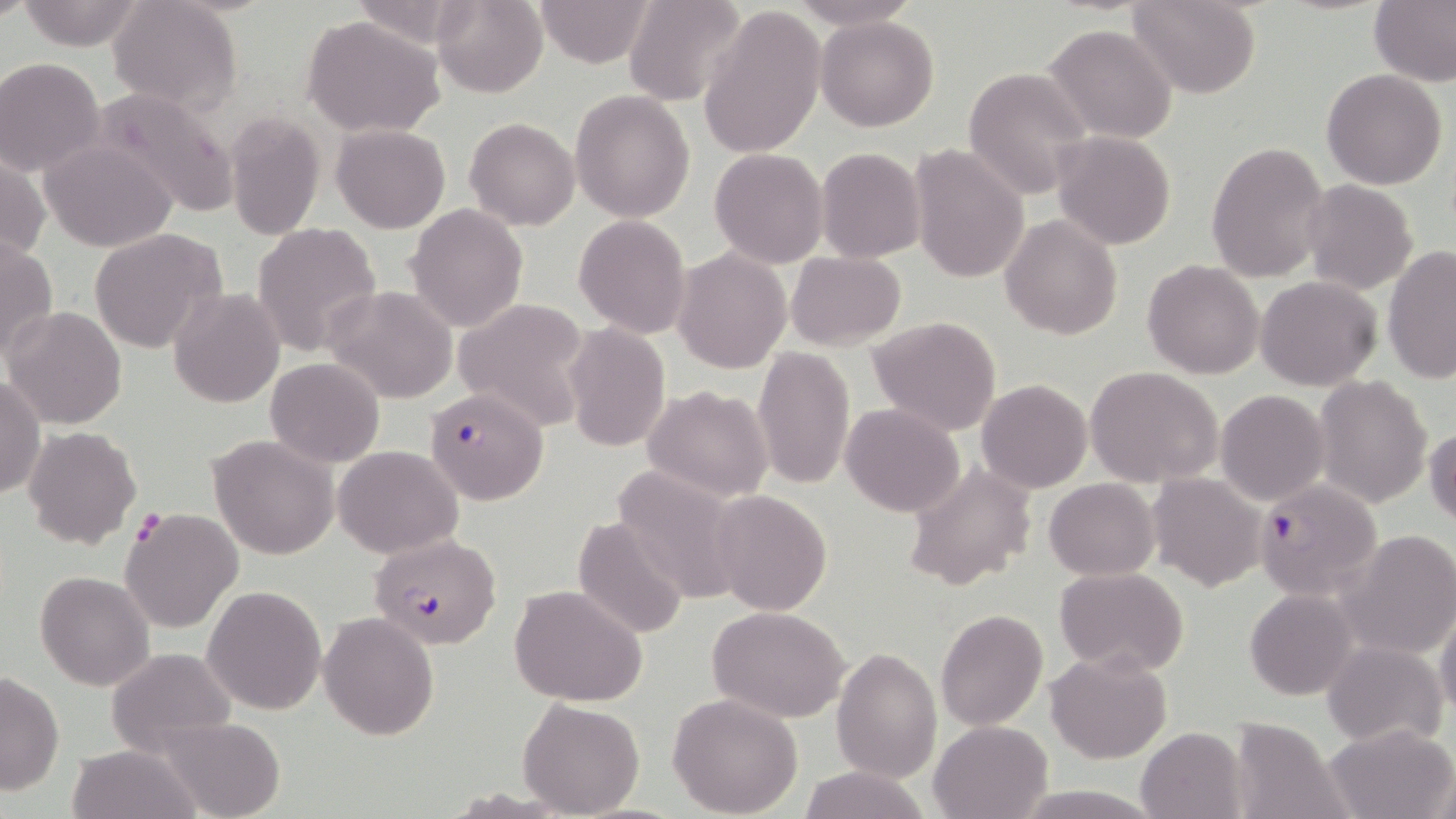
Summary:
  - Coordinate format: approximate bounding boxes as [x1, y1, x2, y2] in pixels
  - Uninfected red blood cell locations: [15, 0, 149, 50], [533, 0, 657, 68], [624, 0, 747, 106], [787, 0, 921, 31], [1129, 0, 1260, 98], [1370, 0, 1456, 87], [105, 1, 243, 116], [431, 1, 548, 95], [699, 5, 827, 156], [302, 16, 445, 137], [816, 16, 939, 131], [1044, 23, 1178, 143], [0, 59, 105, 175], [963, 66, 1091, 200], [1321, 69, 1449, 190], [91, 88, 240, 218], [569, 89, 696, 223], [225, 110, 325, 238], [464, 117, 580, 230], [332, 124, 451, 233], [1053, 130, 1176, 250], [39, 138, 179, 253], [1204, 141, 1329, 283], [815, 146, 925, 263], [911, 146, 1028, 287], [708, 147, 828, 268], [0, 150, 49, 270], [1301, 180, 1417, 294], [405, 204, 528, 332], [574, 214, 690, 338], [1000, 215, 1122, 339], [251, 223, 381, 357], [88, 229, 224, 353], [0, 237, 58, 364], [1382, 245, 1456, 382], [673, 248, 792, 375], [787, 252, 906, 350], [1142, 260, 1265, 379], [1255, 275, 1383, 390], [324, 286, 457, 403], [169, 288, 284, 408], [454, 298, 591, 430], [4, 308, 127, 430], [867, 316, 1002, 435], [562, 323, 671, 452], [753, 346, 855, 490], [265, 357, 385, 466], [1084, 367, 1222, 487], [1, 375, 45, 500], [1313, 375, 1433, 509], [976, 379, 1091, 493], [644, 385, 774, 502], [1216, 389, 1330, 506], [841, 403, 965, 517], [23, 426, 142, 549], [1427, 426, 1456, 530], [208, 433, 339, 559], [333, 445, 463, 559], [610, 463, 746, 604], [903, 464, 1039, 593], [1149, 472, 1265, 590], [1045, 477, 1159, 580], [712, 490, 831, 614], [120, 509, 244, 633], [573, 514, 689, 640], [1342, 530, 1456, 660], [1054, 566, 1189, 678], [35, 571, 156, 690], [202, 585, 326, 715], [508, 585, 648, 707], [1245, 588, 1360, 700], [707, 606, 850, 723], [1436, 608, 1456, 719], [936, 609, 1048, 729], [319, 611, 438, 740], [1322, 641, 1448, 748], [106, 648, 237, 753], [831, 648, 942, 782], [1046, 650, 1170, 763], [0, 671, 64, 794], [667, 692, 804, 818], [518, 699, 645, 818], [153, 717, 284, 815], [1226, 717, 1353, 819], [928, 719, 1055, 818], [1326, 722, 1456, 818], [1136, 727, 1248, 819], [66, 743, 198, 819], [794, 765, 929, 819], [1014, 785, 1157, 818]
  - Plasmodium falciparum-infected red blood cell locations: [425, 388, 549, 505], [1254, 478, 1384, 599], [370, 533, 503, 649]
  - Slide-level diagnosis: Plasmodium falciparum
  - Preparation: thin blood smear
  - Field of view: one of a larger specimen
  - Modality: light microscopy
  - Image size: 1456×819 pixels
  - Stain: May-Grünwald-Giemsa
  - Magnification: 1000x